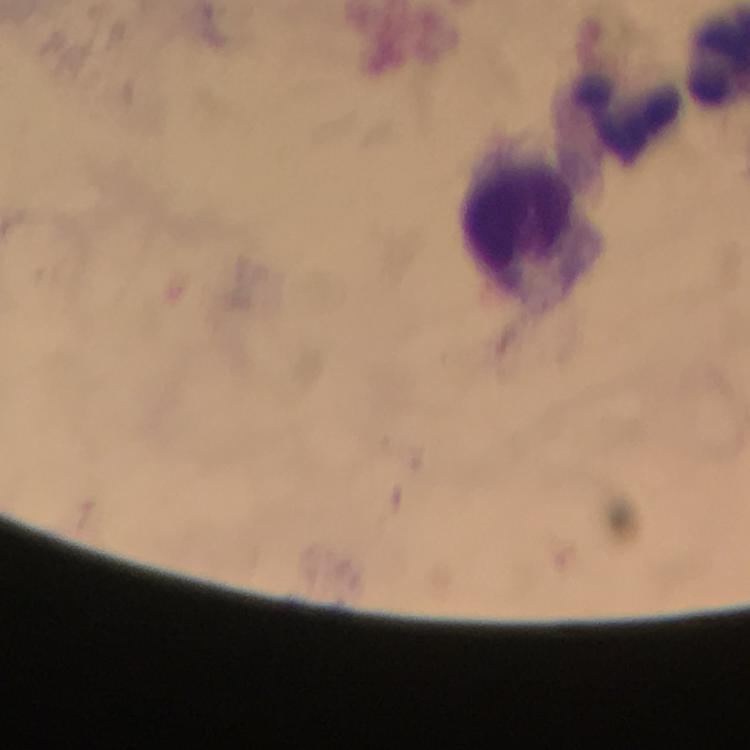

immersion oil = applied
leukocyte locations = approximate centers as (x, y) in pixels: (629, 118), (525, 222)
stain = Giemsa
image size = 750×750 pixels
context = from a diagnostic examination for malaria
cropped from = one field of view
magnification = 100x
capture = smartphone camera through the microscope
Plasmodium parasites = none detected
preparation = thick blood smear